Assess this cell for malaria.
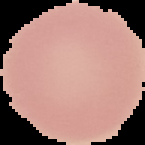
Uninfected.

{
  "image_size": "145×145 pixels",
  "preparation": "thin blood film",
  "image_type": "segmented cell region with the area outside set to black"
}